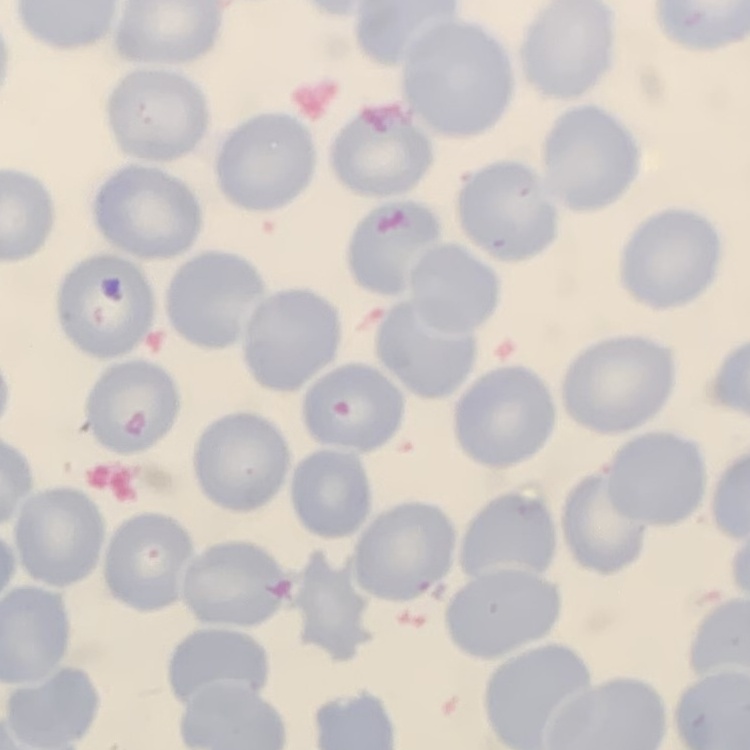 The erythrocytes exhibit no rouleaux formation. One tile cut from a larger photomicrograph. Thin blood smear. Field's or Giemsa stain.